Classify this cell by malaria status.
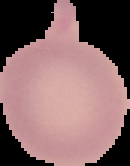
It is uninfected.

Summary:
  - Image type: segmented cell region with the area outside set to black
  - Preparation: thin blood smear
  - Image size: 130×166 pixels